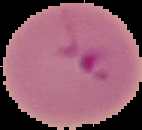

image size = 142×130 pixels
malaria status = parasitized
preparation = thin blood smear
image type = cell region segmented out of the field of view; surrounding area masked to black